Outline each P. falciparum parasite and classify it by life-cycle stage.
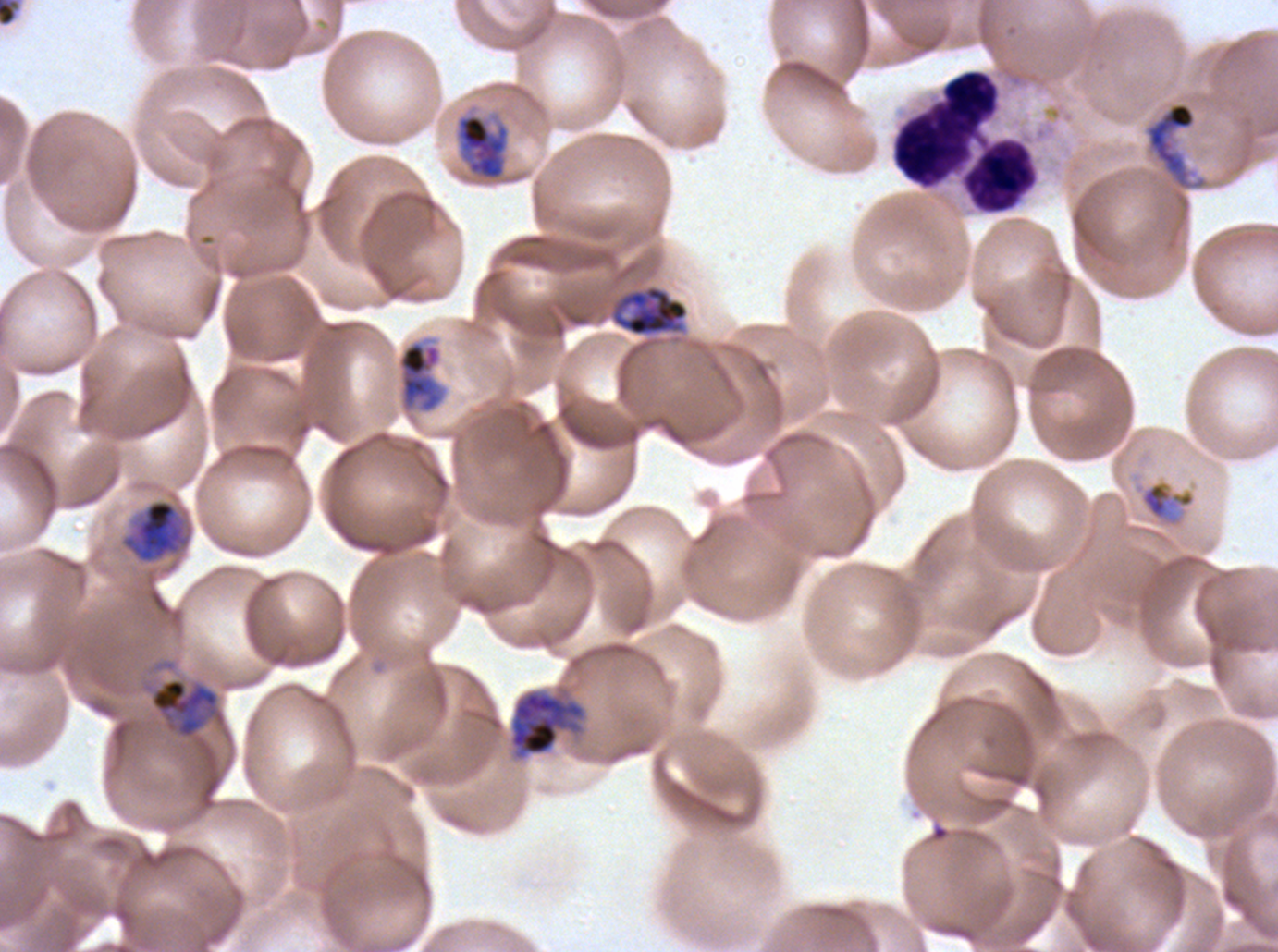

Approximate bounding rectangles given as corner coordinates in pixels from the top-left.
Mid trophozoites: (x1=1139, y1=481, x2=1196, y2=524).
Late trophozoites: (x1=457, y1=114, x2=509, y2=180), (x1=611, y1=285, x2=689, y2=336), (x1=398, y1=340, x2=443, y2=413), (x1=119, y1=498, x2=192, y2=565), (x1=149, y1=677, x2=226, y2=739).
Early schizonts: (x1=1144, y1=101, x2=1207, y2=191), (x1=509, y1=689, x2=586, y2=760).
No rings, late-ring/early-trophozoite forms, late schizonts, segmenters, or gametocytes observed.

Summary:
  - Image size: 1278×952 pixels
  - Life-cycle stages observed: mid trophozoite, late trophozoite, early schizont
  - Specimen: ex-vivo P. falciparum culture from a patient in The Gambia, grown for 24 to 48 hours
  - Preparation: thin blood smear
  - Stain: Giemsa
  - Field of view: one sub-image of a larger composite